Classify this cell by malaria status.
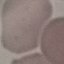

It is uninfected.

{
  "stain": "Giemsa",
  "image_type": "cell patch, automatically extracted from a larger field of view and resized to 64 × 64 pixels",
  "capture": "smartphone camera at the microscope eyepiece",
  "preparation": "thin smear"
}